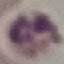
{
  "malaria_status": "uninfected",
  "stain": "Giemsa",
  "image_type": "cell patch, automatically extracted from a larger field of view and resized to 64 × 64 pixels",
  "preparation": "thin blood smear",
  "capture": "smartphone through the microscope eyepiece"
}